Give the position of every leukocyte visible.
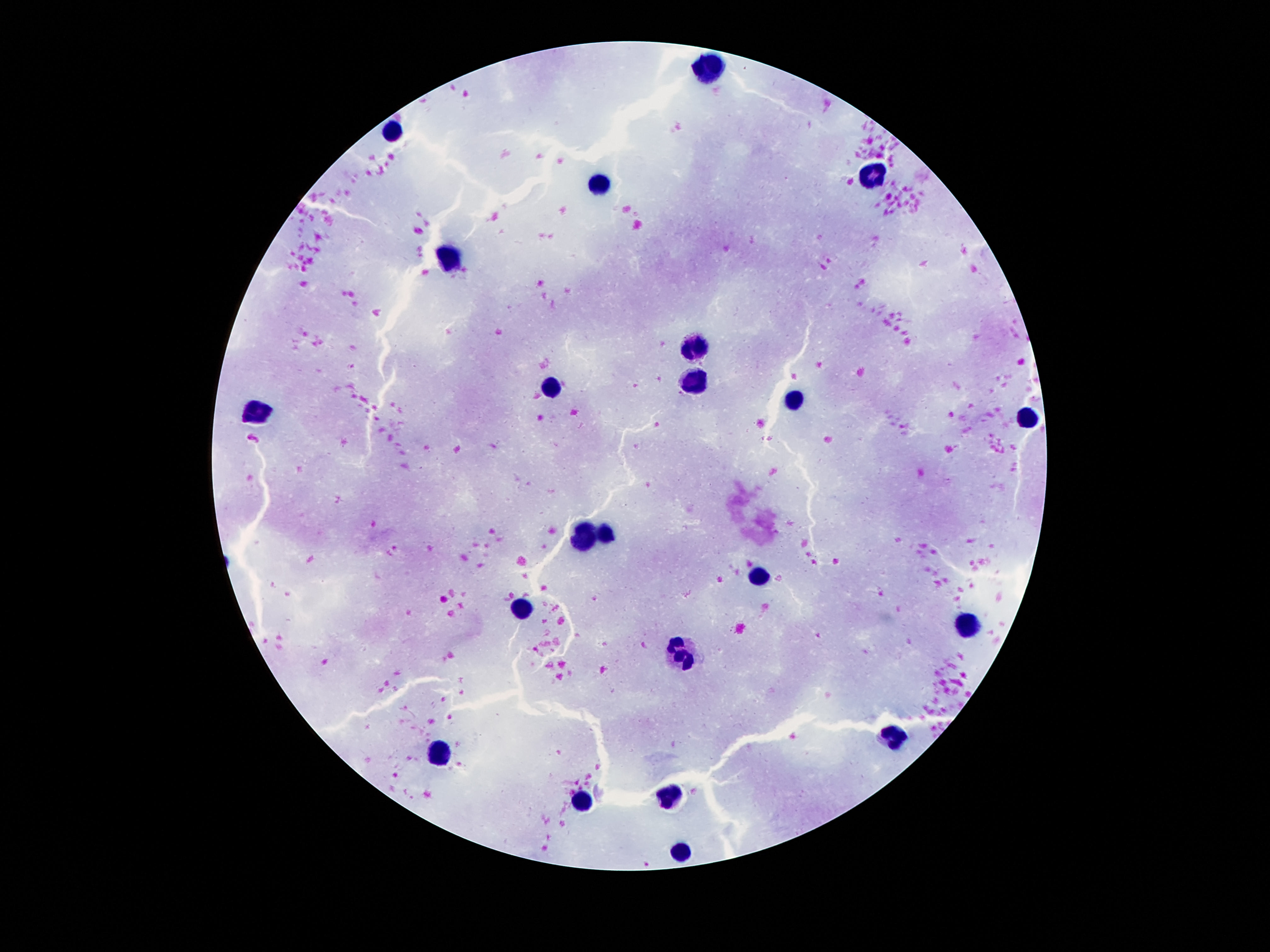

Approximate object centers, in pixels from the top-left corner.
Leukocytes: (x=711, y=68), (x=393, y=130), (x=875, y=177), (x=602, y=184), (x=449, y=256), (x=696, y=345), (x=694, y=377), (x=551, y=384), (x=795, y=401), (x=257, y=411), (x=1028, y=419), (x=607, y=536), (x=583, y=537), (x=759, y=578), (x=523, y=607), (x=965, y=624), (x=684, y=652), (x=894, y=736), (x=442, y=753), (x=670, y=799), (x=581, y=804), (x=681, y=851).

image size = 1270×952 pixels
field of view = one from this slide
magnification = 100x
capture = smartphone camera through the microscope eyepiece
preparation = thick blood smear
stain = Giemsa
patient malaria status = uninfected